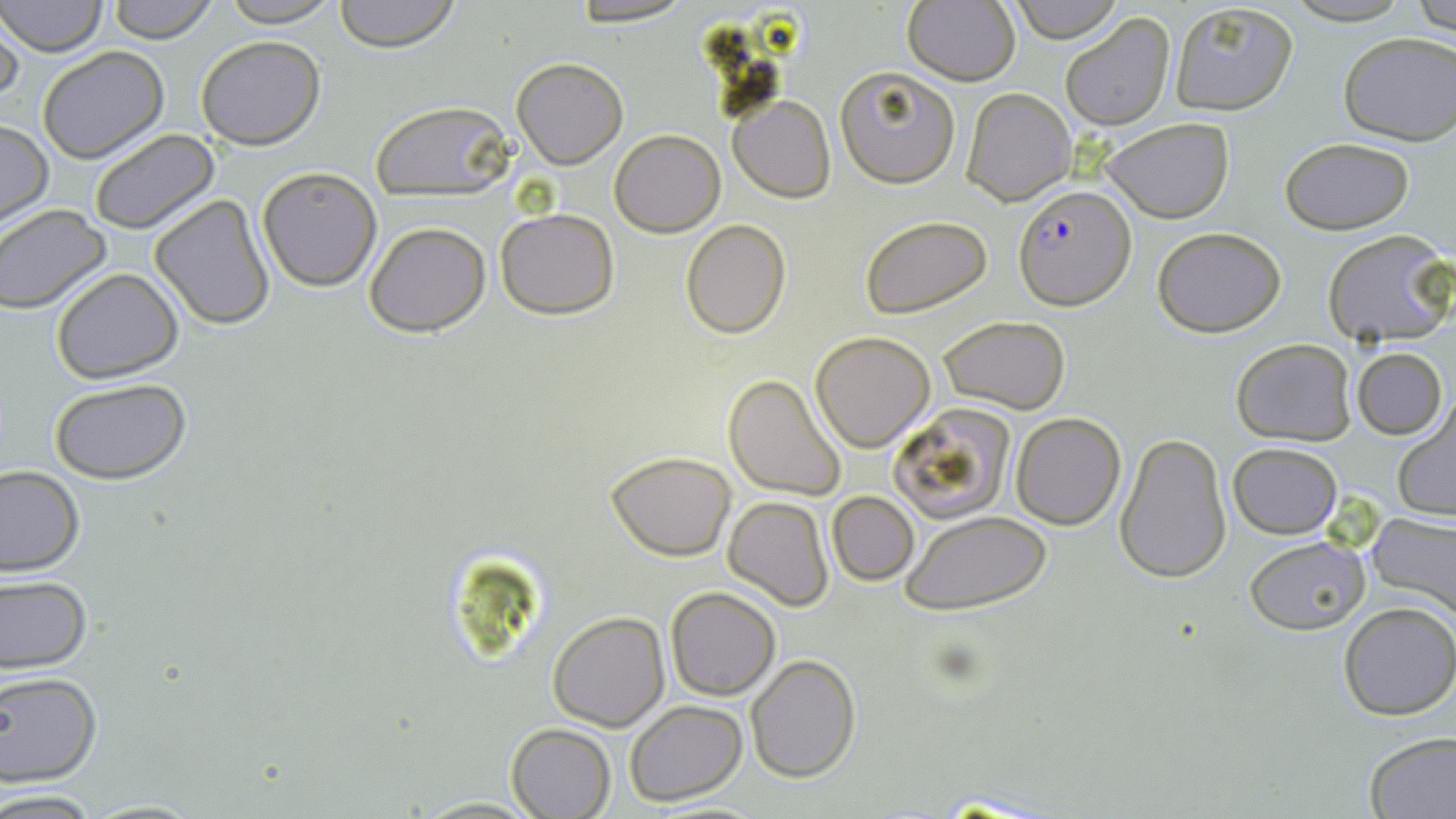
Summary:
  - Coordinate format: approximate bounding boxes as (x1, y1, x2, y2) in pixels
  - Plasmodium falciparum-infected red blood cell locations: (1015, 184, 1135, 311)
  - Uninfected red blood cell locations: (2, 0, 107, 56), (107, 0, 218, 43), (218, 0, 344, 26), (333, 0, 461, 51), (562, 0, 699, 26), (1009, 0, 1125, 43), (1279, 0, 1413, 25), (1412, 0, 1456, 35), (1168, 2, 1299, 115), (903, 3, 1020, 85), (0, 9, 23, 102), (1060, 13, 1175, 131), (1337, 32, 1455, 145), (194, 36, 326, 150), (37, 46, 169, 165), (511, 57, 627, 169), (835, 66, 960, 188), (960, 87, 1076, 207), (728, 95, 836, 202), (370, 101, 515, 200), (1101, 117, 1235, 222), (0, 119, 52, 229), (89, 128, 220, 235), (609, 129, 724, 237), (1279, 137, 1415, 235), (257, 166, 382, 292), (149, 194, 276, 330), (0, 205, 112, 313), (494, 207, 619, 318), (860, 215, 993, 318), (680, 219, 790, 338), (365, 221, 490, 335), (1152, 226, 1286, 338), (1321, 229, 1454, 349), (50, 268, 184, 384), (937, 316, 1071, 414), (809, 332, 935, 452), (1232, 338, 1356, 447), (1353, 347, 1446, 439), (723, 374, 847, 501), (48, 379, 193, 485), (1391, 400, 1456, 524), (888, 403, 1016, 523), (1010, 412, 1126, 529), (1114, 431, 1233, 585), (1227, 442, 1342, 538), (606, 451, 735, 561), (0, 465, 84, 577), (827, 491, 918, 584), (723, 496, 833, 610), (901, 509, 1051, 616), (1366, 509, 1456, 623), (1244, 536, 1367, 636), (0, 576, 92, 675), (666, 586, 781, 700), (1338, 603, 1455, 720), (548, 610, 670, 731), (745, 654, 862, 783), (0, 672, 102, 787), (625, 701, 749, 802), (507, 723, 615, 817), (1360, 732, 1456, 819), (0, 788, 103, 816), (925, 789, 1066, 817), (80, 797, 206, 817), (642, 802, 775, 818)
  - Slide-level diagnosis: Plasmodium falciparum
  - Preparation: thin blood smear
  - Stain: May-Grünwald-Giemsa
  - Modality: optical microscopy
  - Magnification: 1000x
  - Image size: 1456×819 pixels
  - Field of view: one of a larger specimen